Assess this cell for malaria.
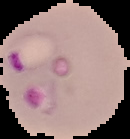

Parasitized.

preparation: thin blood smear
image_type: cell region segmented out of the field of view; surrounding area masked to black
image_size: 130×139 pixels